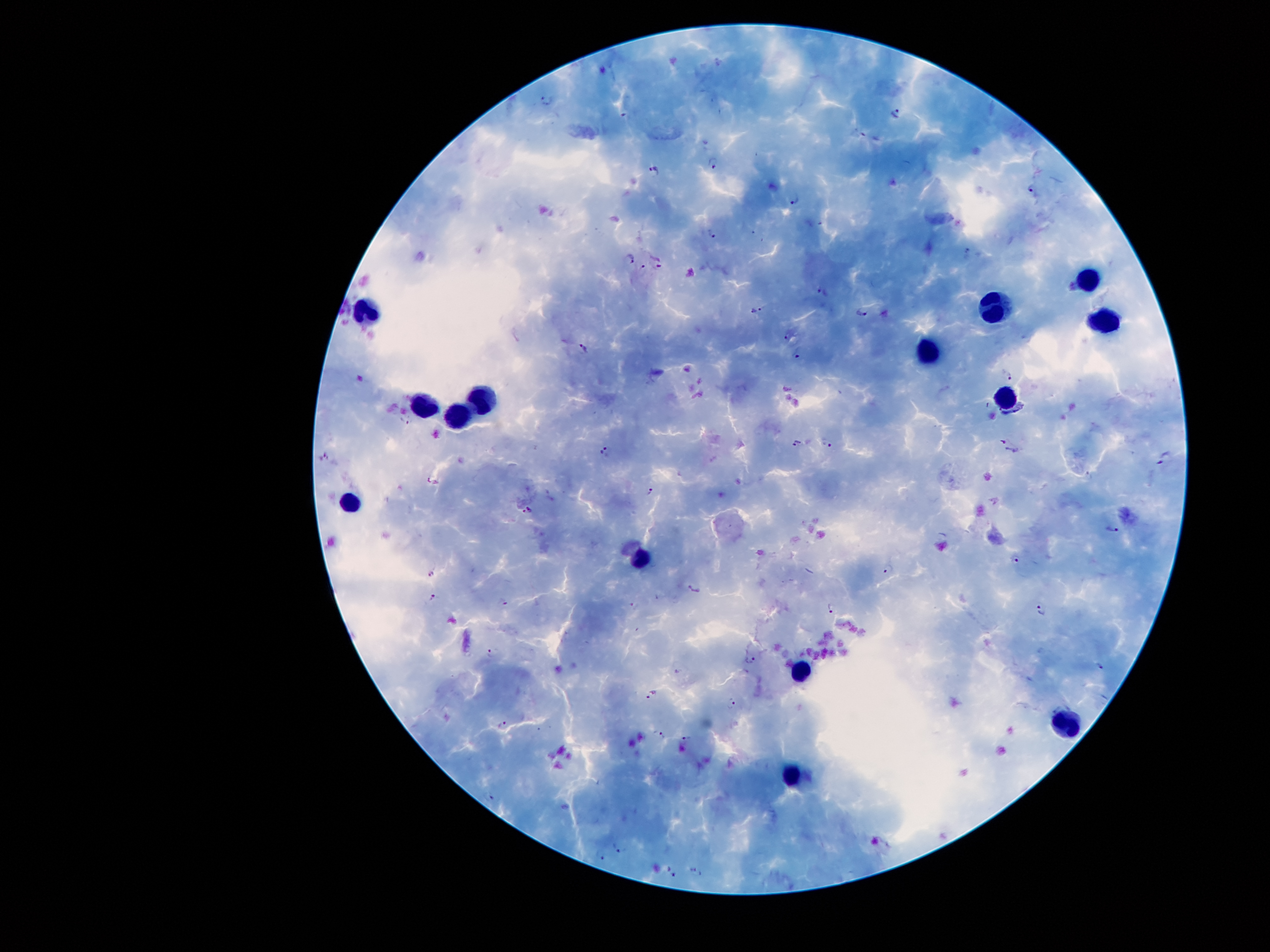
Approximate centers as [x, y] in pixels. Leukocyte locations: [1087, 275], [996, 309], [368, 320], [1102, 321], [927, 350], [482, 396], [1003, 396], [424, 404], [456, 411], [347, 500], [640, 558], [800, 669], [1064, 721], [791, 773]. Malaria parasite locations: [547, 99], [896, 113], [627, 116], [712, 163], [654, 169], [1031, 188], [795, 198], [710, 233], [630, 257], [659, 265], [642, 267], [822, 293], [757, 310], [862, 311], [788, 336], [584, 347], [799, 354], [1008, 375], [405, 421], [798, 442], [829, 443], [1008, 447], [606, 451], [324, 456], [1164, 458], [652, 491], [526, 510], [1113, 529], [1016, 559], [889, 568], [430, 574], [694, 589], [432, 599], [503, 602], [634, 606], [832, 608], [1042, 610], [488, 654], [752, 659], [1099, 667], [653, 693], [732, 703], [502, 723], [660, 735], [687, 738], [489, 798], [621, 847], [599, 858], [671, 872], [696, 872]. Giemsa-stained preparation. Smartphone photograph taken through the microscope eyepiece. Single field of view. Patient malaria status: positive for Plasmodium falciparum. Image is 1270×952 pixels. Thick peripheral-blood smear. 100x magnification.